Assess the morphology of the red blood cells.
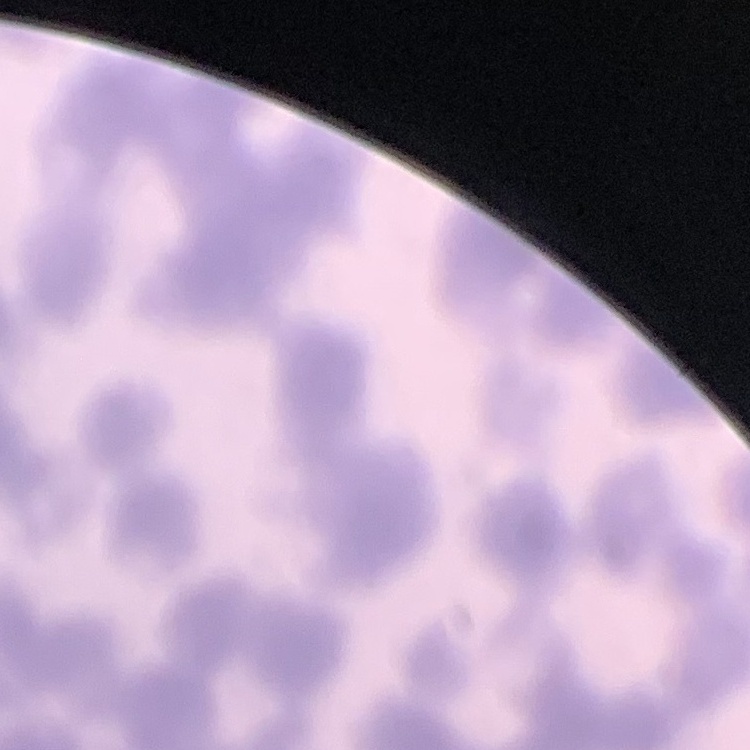

They show rouleaux formation.

image_type: one tile cut from a larger photomicrograph
preparation: thin blood film
stain: Field's or Giemsa